Outline each blood parasite and name the species.
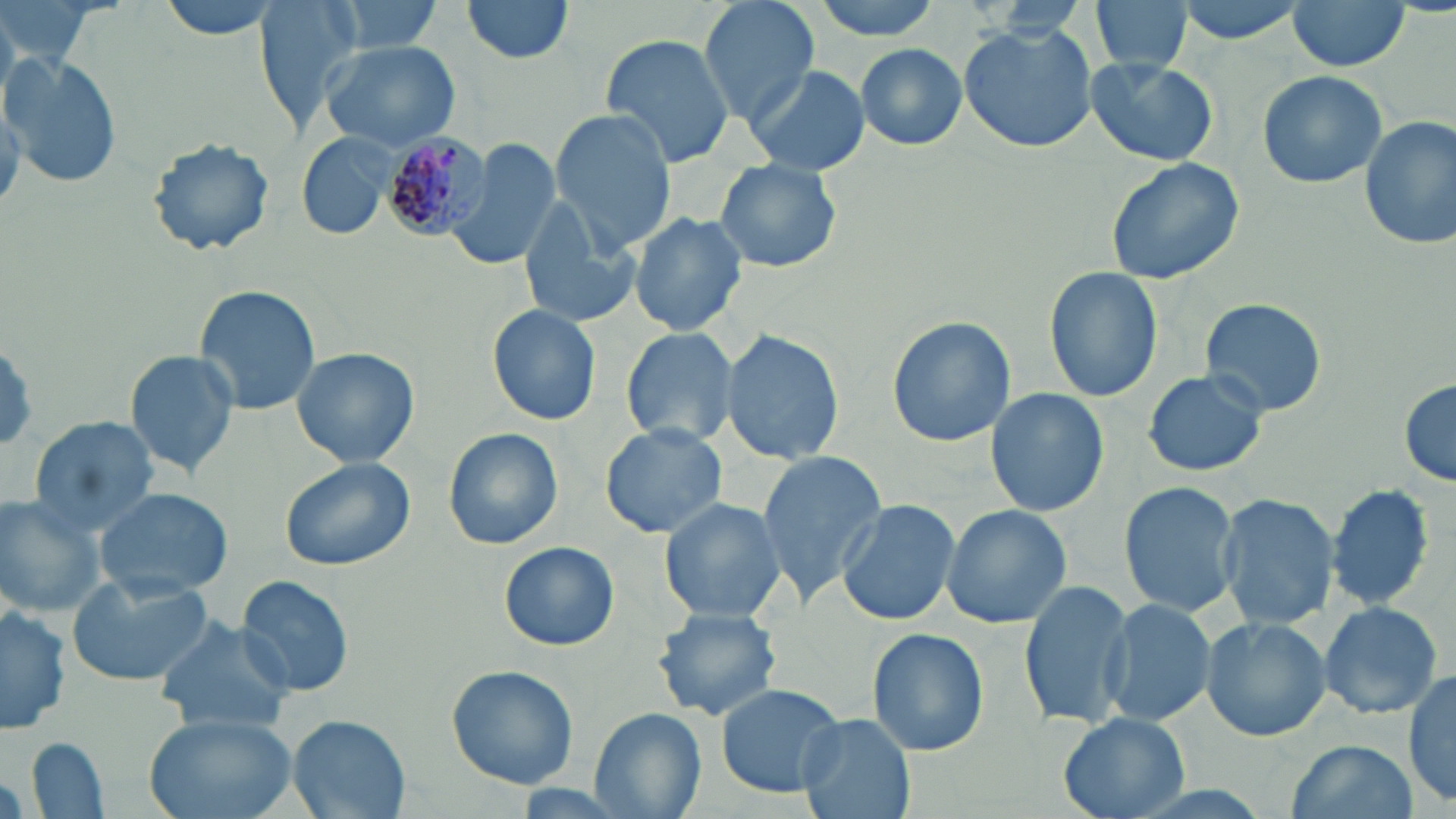

Approximate bounding boxes as (x1, y1, x2, y2) in pixels.
Plasmodium malariae-infected red blood cells: (381, 133, 490, 240).
No Plasmodium falciparum, Plasmodium ovale, Plasmodium vivax, Babesia divergens, or Trypanosoma brucei observed.

slide-level diagnosis = Plasmodium malariae
image size = 1456×819 pixels
uninfected red blood cell locations = approximate bounding boxes as (x1, y1, x2, y2) in pixels: (155, 0, 287, 39), (252, 0, 364, 134), (697, 0, 820, 125), (802, 0, 949, 40), (1089, 0, 1194, 73), (1170, 0, 1313, 44), (462, 1, 575, 66), (1282, 1, 1411, 72), (959, 20, 1101, 153), (599, 32, 737, 171), (321, 41, 462, 152), (856, 42, 968, 150), (4, 56, 121, 187), (1085, 57, 1218, 165), (746, 64, 869, 176), (1256, 70, 1387, 189), (550, 111, 677, 256), (1358, 115, 1456, 253), (296, 133, 397, 241), (147, 136, 275, 257), (447, 140, 560, 272), (716, 157, 842, 275), (1102, 158, 1245, 285), (515, 198, 643, 331), (628, 210, 748, 337), (1043, 267, 1163, 403), (193, 284, 322, 416), (1199, 296, 1327, 418), (486, 303, 601, 426), (887, 315, 1017, 448), (719, 325, 849, 467), (621, 326, 740, 448), (290, 347, 421, 468), (125, 348, 241, 478), (1141, 369, 1269, 478), (1397, 378, 1456, 488), (986, 389, 1108, 517), (27, 416, 159, 536), (598, 423, 728, 538), (443, 427, 563, 550), (756, 452, 887, 606), (281, 459, 416, 571), (1119, 481, 1241, 616), (1326, 483, 1437, 613), (93, 487, 235, 598), (1214, 493, 1340, 630), (0, 495, 103, 617), (659, 497, 787, 624), (836, 498, 959, 625), (941, 505, 1072, 629), (498, 541, 620, 651), (66, 571, 216, 689), (236, 574, 355, 699), (1018, 579, 1135, 730), (1100, 598, 1214, 728), (1316, 600, 1442, 719), (0, 604, 71, 738), (653, 606, 781, 721), (155, 616, 298, 735), (1201, 616, 1331, 741), (866, 628, 990, 758), (445, 665, 580, 790), (1406, 666, 1456, 809), (716, 683, 846, 797), (590, 707, 706, 819), (144, 710, 299, 819), (1059, 710, 1190, 818), (289, 713, 410, 818), (795, 714, 916, 819), (29, 737, 110, 817), (1282, 738, 1418, 819)
field of view = one of a larger specimen
magnification = 1000x
preparation = thin blood film
modality = light microscopy
stain = May-Grünwald-Giemsa